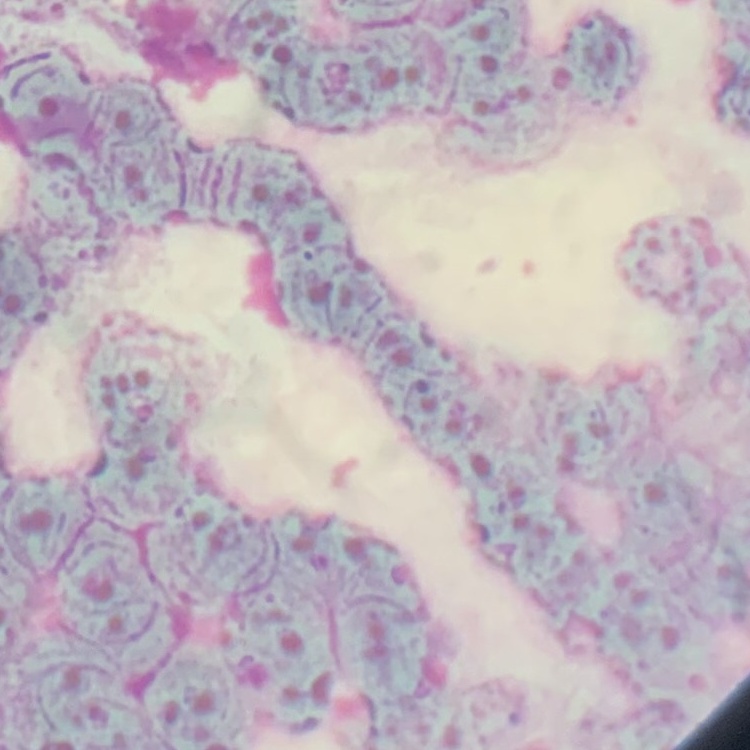

The erythrocytes exhibit rouleaux formation. Square crop of a larger photomicrograph. Thin blood smear. Field's or Giemsa stain.